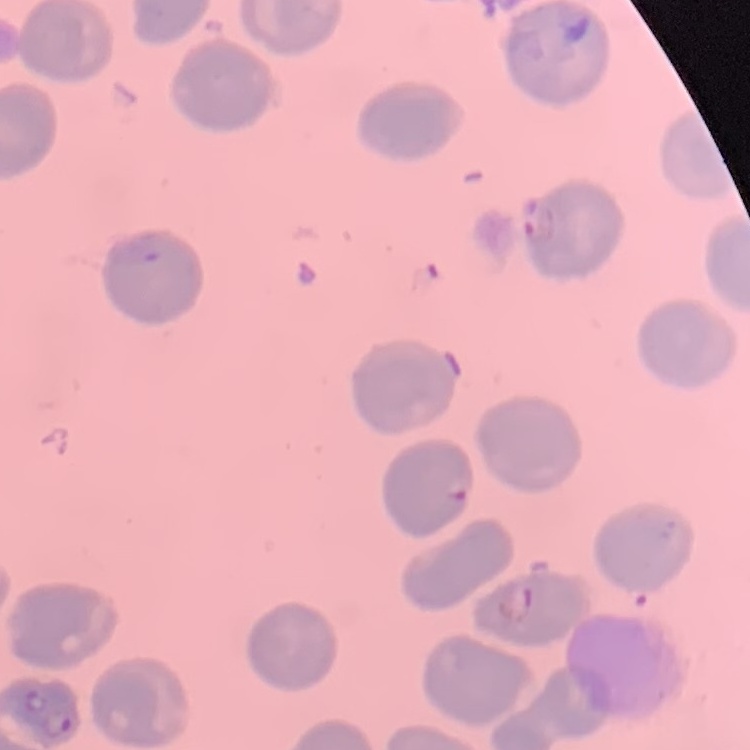

The red blood cells exhibit no rouleaux formation. Stained with either Field's or Giemsa. One tile cut from a larger photomicrograph. Thin peripheral smear.